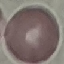

Summary:
  - Malaria status: uninfected
  - Stain: Giemsa
  - Image type: automatically extracted cell patch, resized to 64 × 64 pixels
  - Capture: smartphone through the microscope eyepiece
  - Preparation: thin blood smear